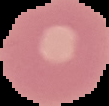

Summary:
  - Malaria status: uninfected
  - Image size: 109×106 pixels
  - Preparation: thin blood film
  - Image type: segmented cell region on a black background